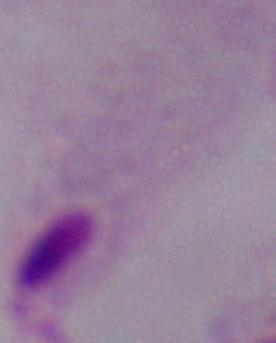

Summary:
  - Identification: trichomonad
  - Modality: micrograph
  - Magnification: 1000x